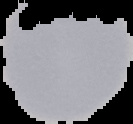

Result: no malaria parasites seen. From a thin blood smear. Segmented cell region on a black background. Image is 133×124 pixels.